Identify the parasite.
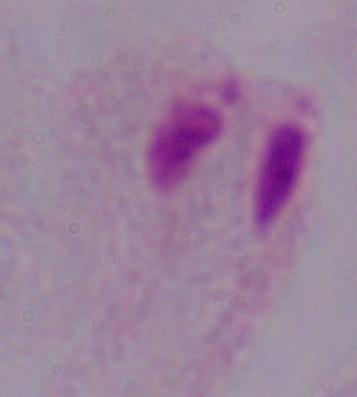

This is a trichomonad.

Micrograph. 1000x magnification.